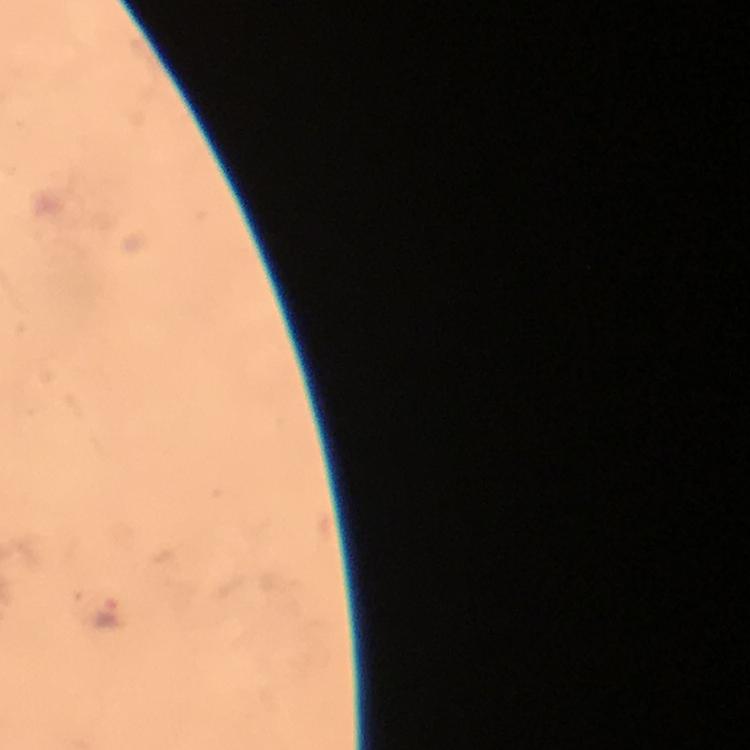
magnification = 100x
Plasmodium parasite locations = approximate centers as [x, y] in pixels: [106, 617]
stain = Giemsa
immersion oil = applied
capture = smartphone camera through the microscope
image size = 750×750 pixels
preparation = thick blood smear
cropped from = one field of view
context = from a diagnostic examination for malaria